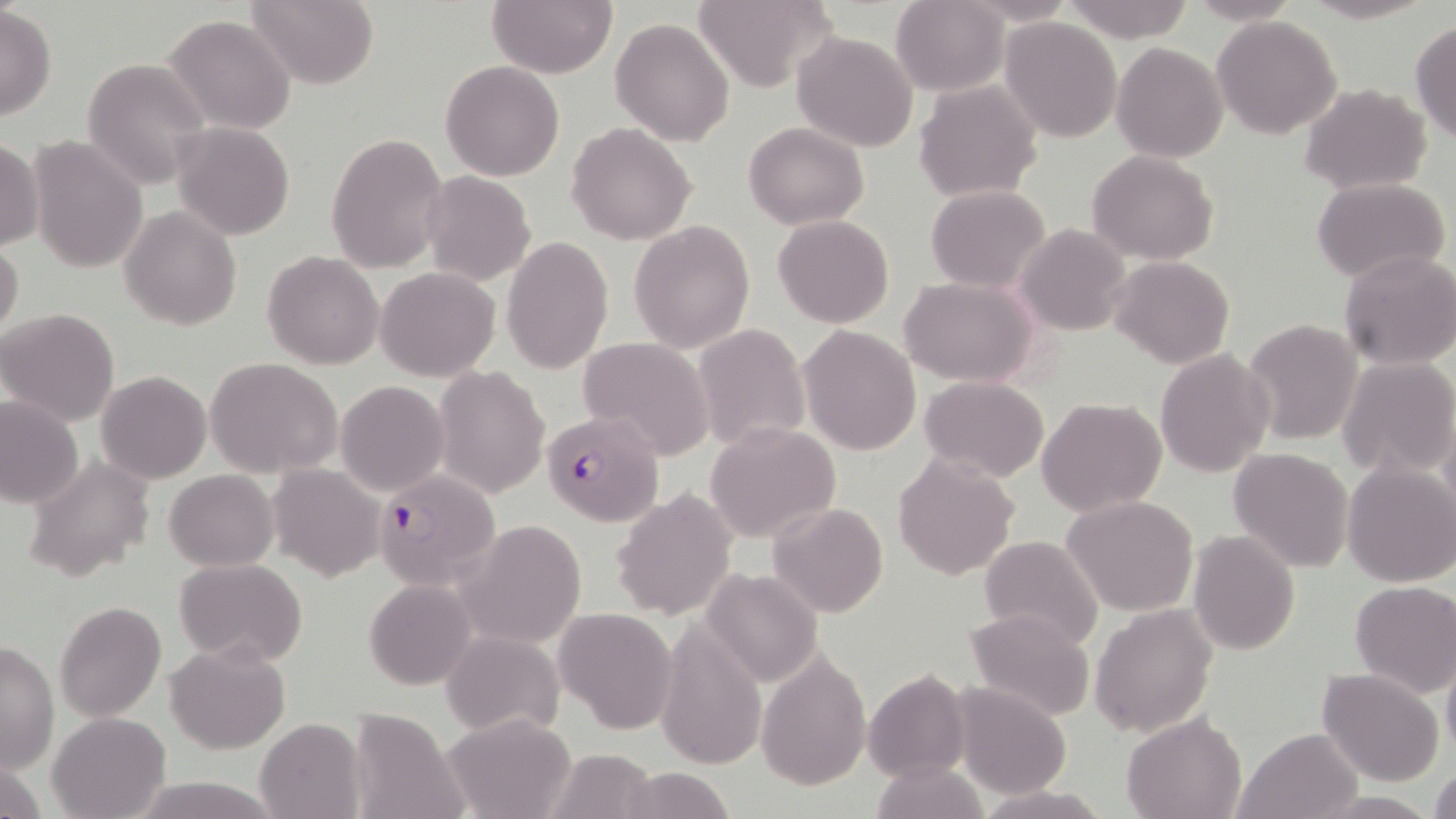
Plasmodium falciparum-infected red blood cell locations = approximate bounding boxes as (x1,y1)-(x2,y2) corner pairs in pixels: (542,411)-(664,527), (373,470)-(501,590)
slide-level diagnosis = Plasmodium falciparum
preparation = thin blood smear
image size = 1456×819 pixels
uninfected red blood cell locations = approximate bounding boxes as (x1,y1)-(x2,y2) corner pairs in pixels: (891,0)-(1010,96), (1061,0)-(1195,41), (1186,0)-(1302,25), (1296,0)-(1436,24), (246,1)-(378,88), (488,1)-(617,77), (694,1)-(841,90), (0,6)-(57,121), (162,14)-(296,134), (1211,15)-(1343,140), (1001,17)-(1123,142), (611,18)-(733,146), (1409,21)-(1456,144), (791,31)-(917,152), (1112,42)-(1227,164), (84,58)-(212,191), (441,61)-(565,182), (913,82)-(1043,201), (1301,83)-(1431,194), (172,120)-(294,240), (566,122)-(696,244), (743,123)-(870,229), (327,132)-(449,274), (26,134)-(148,274), (0,139)-(44,251), (1087,150)-(1219,264), (422,172)-(536,287), (1311,177)-(1450,284), (926,185)-(1050,294), (119,206)-(240,330), (773,215)-(893,328), (629,220)-(756,355), (1016,224)-(1131,336), (502,236)-(613,373), (0,239)-(24,344), (1337,250)-(1455,369), (263,251)-(383,369), (1109,255)-(1235,370), (376,267)-(501,382), (901,277)-(1039,386), (0,307)-(121,426), (1242,319)-(1363,445), (692,323)-(811,451), (798,326)-(922,456), (577,337)-(715,458), (1155,348)-(1275,476), (1337,356)-(1456,481), (206,358)-(344,478), (434,365)-(550,501), (96,370)-(212,483), (919,375)-(1050,482), (336,380)-(449,496), (0,394)-(84,508), (1035,396)-(1167,517), (705,422)-(841,543), (1228,446)-(1352,572), (892,453)-(1020,580), (23,454)-(156,582), (1341,461)-(1456,587), (269,464)-(385,582), (165,470)-(278,571), (612,488)-(738,620), (1062,494)-(1200,616), (769,502)-(889,617), (457,519)-(586,650), (1188,530)-(1300,658), (978,535)-(1104,649), (174,557)-(307,667), (700,566)-(825,689), (365,577)-(478,690), (1349,580)-(1456,698), (54,600)-(167,722), (1089,605)-(1217,737), (554,607)-(677,735), (963,609)-(1096,721), (654,617)-(768,772), (443,630)-(565,738), (165,641)-(290,753), (1,642)-(59,776), (756,650)-(868,791), (1441,656)-(1456,760), (1318,668)-(1444,787), (863,669)-(972,783), (950,683)-(1072,799), (346,707)-(470,819), (47,712)-(170,819), (440,713)-(578,819), (1122,713)-(1246,819), (254,717)-(365,819), (1233,728)-(1362,818), (546,747)-(660,819), (870,759)-(986,819), (1430,764)-(1456,819), (615,766)-(738,819), (127,776)-(284,817), (973,785)-(1113,818)
modality = optical microscopy
magnification = 1000x
stain = May-Grünwald-Giemsa
field of view = one of a larger specimen